Classify this cell by malaria status.
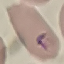
Parasitized.

Giemsa stain. Cell patch, automatically extracted from a larger field of view and resized to 64 × 64 pixels. Photographed with a smartphone camera at the microscope eyepiece. Thin blood smear.